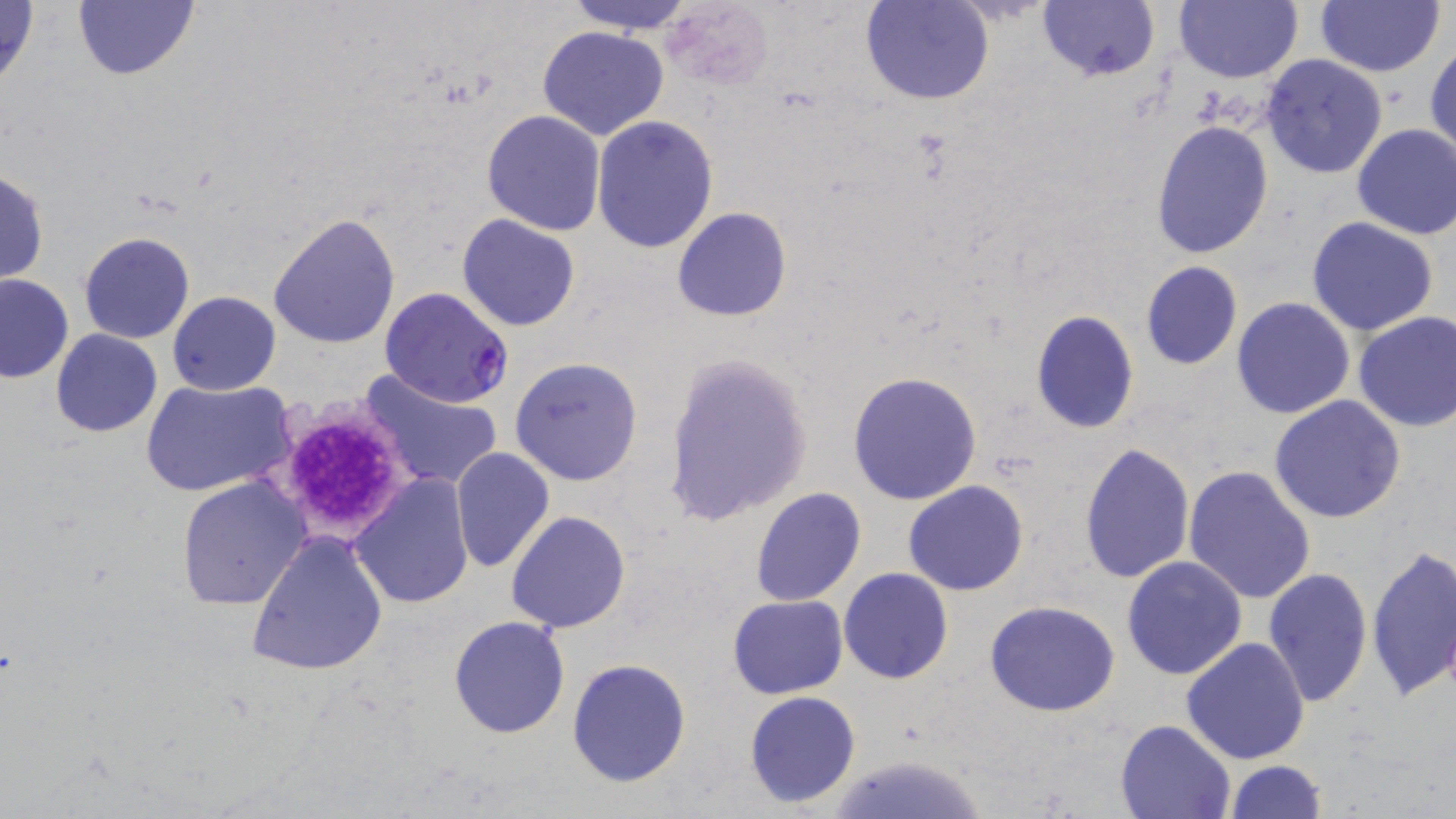 Approximate bounding boxes as (x1, y1, x2, y2) in pixels. Uninfected red blood cell locations: (0, 0, 40, 92), (72, 0, 198, 81), (563, 0, 697, 34), (863, 0, 994, 105), (1037, 0, 1159, 82), (1175, 0, 1301, 84), (1315, 0, 1445, 76), (661, 2, 771, 88), (537, 25, 669, 139), (1426, 40, 1456, 163), (1259, 52, 1387, 178), (482, 110, 606, 236), (591, 116, 719, 253), (1150, 119, 1275, 258), (1351, 123, 1456, 240), (0, 167, 50, 286), (671, 206, 792, 323), (268, 211, 401, 348), (456, 213, 582, 332), (1306, 216, 1439, 336), (79, 231, 196, 344), (1139, 261, 1243, 371), (0, 272, 73, 383), (168, 290, 280, 395), (1231, 297, 1357, 420), (1030, 309, 1139, 432), (1352, 311, 1456, 432), (50, 329, 161, 437), (662, 352, 813, 524), (509, 356, 643, 486), (848, 371, 982, 505), (359, 372, 505, 492), (142, 377, 296, 497), (1267, 395, 1407, 523), (1079, 441, 1194, 584), (449, 446, 555, 574), (1184, 464, 1316, 604), (348, 474, 474, 609), (177, 476, 310, 609), (903, 480, 1029, 596), (750, 488, 866, 606), (506, 510, 631, 634), (247, 529, 388, 676), (1365, 545, 1456, 702), (1121, 555, 1249, 680), (838, 567, 953, 685), (1263, 568, 1373, 707), (727, 595, 848, 700), (985, 602, 1121, 717), (447, 615, 570, 738), (1181, 636, 1312, 765), (567, 659, 692, 787), (743, 691, 860, 809), (1114, 718, 1237, 818), (827, 752, 988, 819), (1223, 760, 1327, 819). Plasmodium falciparum-infected red blood cell locations: (379, 286, 513, 408). Platelet locations: (269, 398, 416, 544). Slide-level diagnosis: Plasmodium falciparum. Optical microscopy. Thin blood film. Image is 1456×819 pixels. One field of a larger specimen. 1000x magnification. May-Grünwald-Giemsa stain.